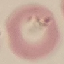

Summary:
  - Result: malaria parasites detected
  - Stain: Giemsa
  - Preparation: thin smear
  - Image type: automatically extracted cell patch, resized to 64 × 64 pixels
  - Capture: smartphone through the microscope eyepiece